Report the malaria status of this cell.
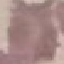
It is uninfected.

preparation = thin smear
capture = smartphone camera at the microscope eyepiece
stain = Giemsa
image type = automatically extracted cell patch, resized to 64 × 64 pixels